State the blood parasite species.
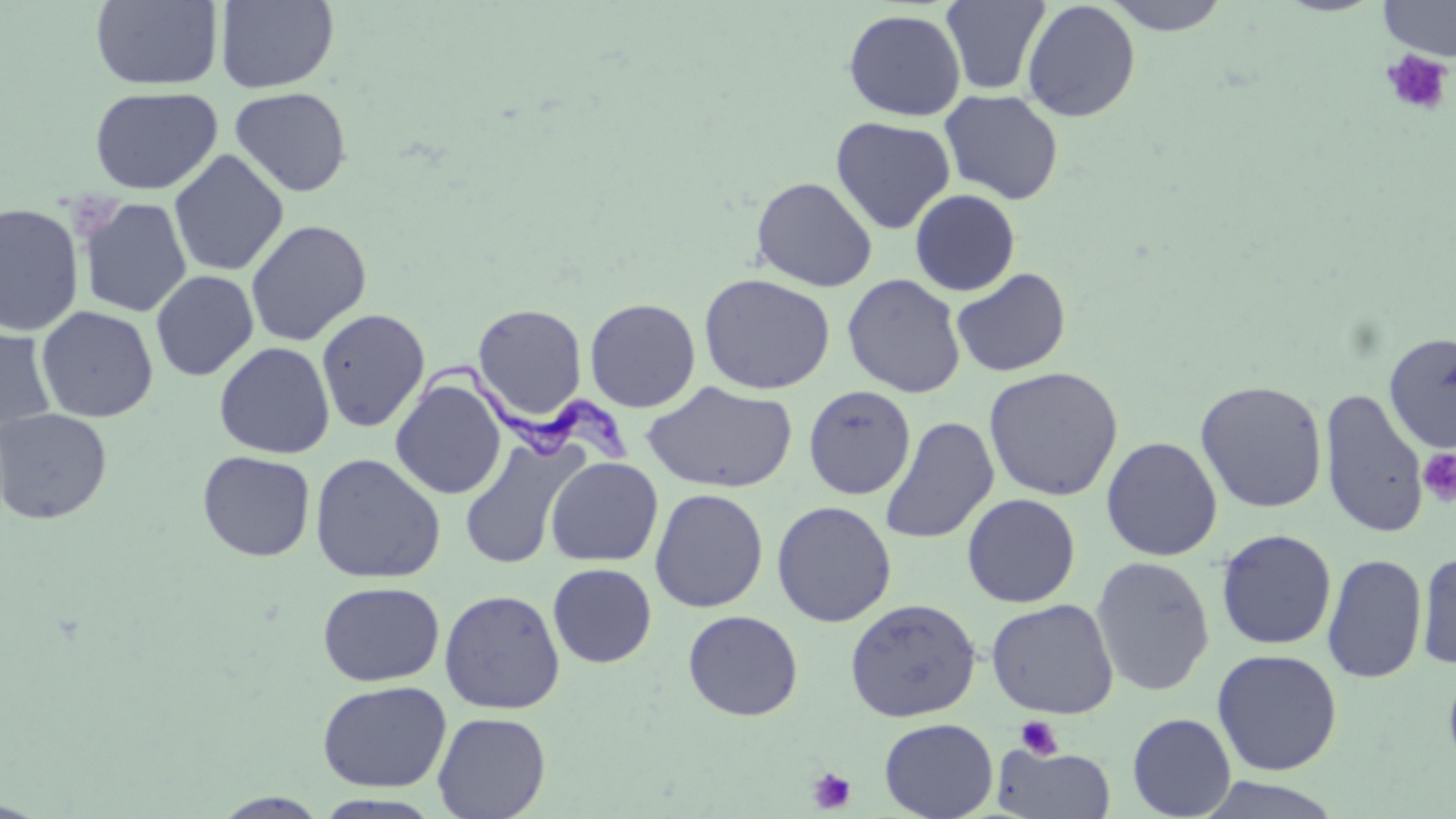

Trypanosoma brucei.

{
  "platelet_locations": "approximate bounding boxes as [x1, y1, x2, y2] in pixels: [1380, 48, 1454, 117], [1417, 448, 1456, 506], [1015, 716, 1063, 759], [806, 767, 857, 814]",
  "modality": "light microscopy",
  "preparation": "thin blood smear",
  "magnification": "1000x",
  "field_of_view": "single",
  "image_size": "1456×819 pixels",
  "stain": "May-Grünwald-Giemsa",
  "uninfected_red_blood_cell_locations": "approximate bounding boxes as [x1, y1, x2, y2] in pixels: [91, 0, 223, 90], [215, 0, 339, 93], [940, 0, 1051, 95], [1100, 0, 1233, 35], [1378, 0, 1456, 60], [1021, 1, 1140, 122], [843, 9, 966, 121], [89, 86, 222, 196], [229, 87, 352, 197], [939, 90, 1064, 205], [830, 116, 955, 234], [169, 149, 289, 277], [751, 176, 878, 292], [909, 189, 1020, 296], [78, 198, 192, 317], [0, 203, 84, 336], [245, 220, 372, 346], [951, 267, 1071, 378], [150, 270, 259, 381], [698, 272, 836, 395], [842, 274, 966, 398], [585, 298, 701, 412], [472, 303, 587, 423], [36, 306, 158, 423], [315, 308, 430, 432], [0, 324, 57, 438], [1384, 333, 1456, 454], [214, 341, 335, 459], [983, 366, 1123, 501], [390, 377, 506, 499], [642, 380, 798, 494], [1195, 380, 1328, 513], [803, 385, 916, 500], [1319, 387, 1430, 539], [0, 408, 113, 525], [879, 416, 999, 544], [1101, 436, 1223, 561], [459, 437, 584, 570], [197, 450, 316, 561], [309, 452, 446, 584], [546, 457, 663, 566], [649, 488, 768, 613], [962, 493, 1081, 608], [771, 500, 897, 627], [1216, 528, 1337, 650], [1415, 549, 1456, 670], [1322, 553, 1427, 684], [1090, 555, 1215, 697], [547, 563, 657, 668], [317, 581, 444, 686], [439, 589, 565, 714], [844, 597, 981, 722], [985, 598, 1120, 719], [683, 610, 803, 721], [1211, 649, 1343, 776], [1442, 661, 1456, 779], [317, 680, 451, 792], [432, 711, 551, 819], [1127, 712, 1237, 819], [879, 718, 999, 819], [992, 745, 1116, 818], [1194, 777, 1348, 819], [211, 792, 332, 818], [310, 793, 447, 818]",
  "trypanosoma_brucei_locations": "approximate bounding boxes as [x1, y1, x2, y2] in pixels: [406, 356, 636, 473]"
}